Assess the morphology of the red blood cells.
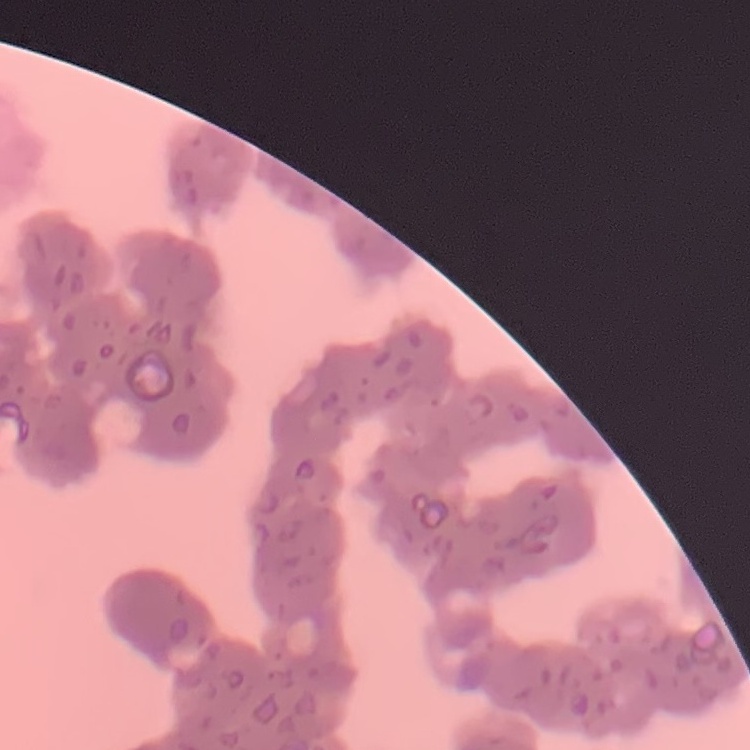
Rouleaux formation.

One tile cut from a larger photomicrograph. Thin blood film. Stained with either Field's or Giemsa.